Outline each blood parasite and name the species.
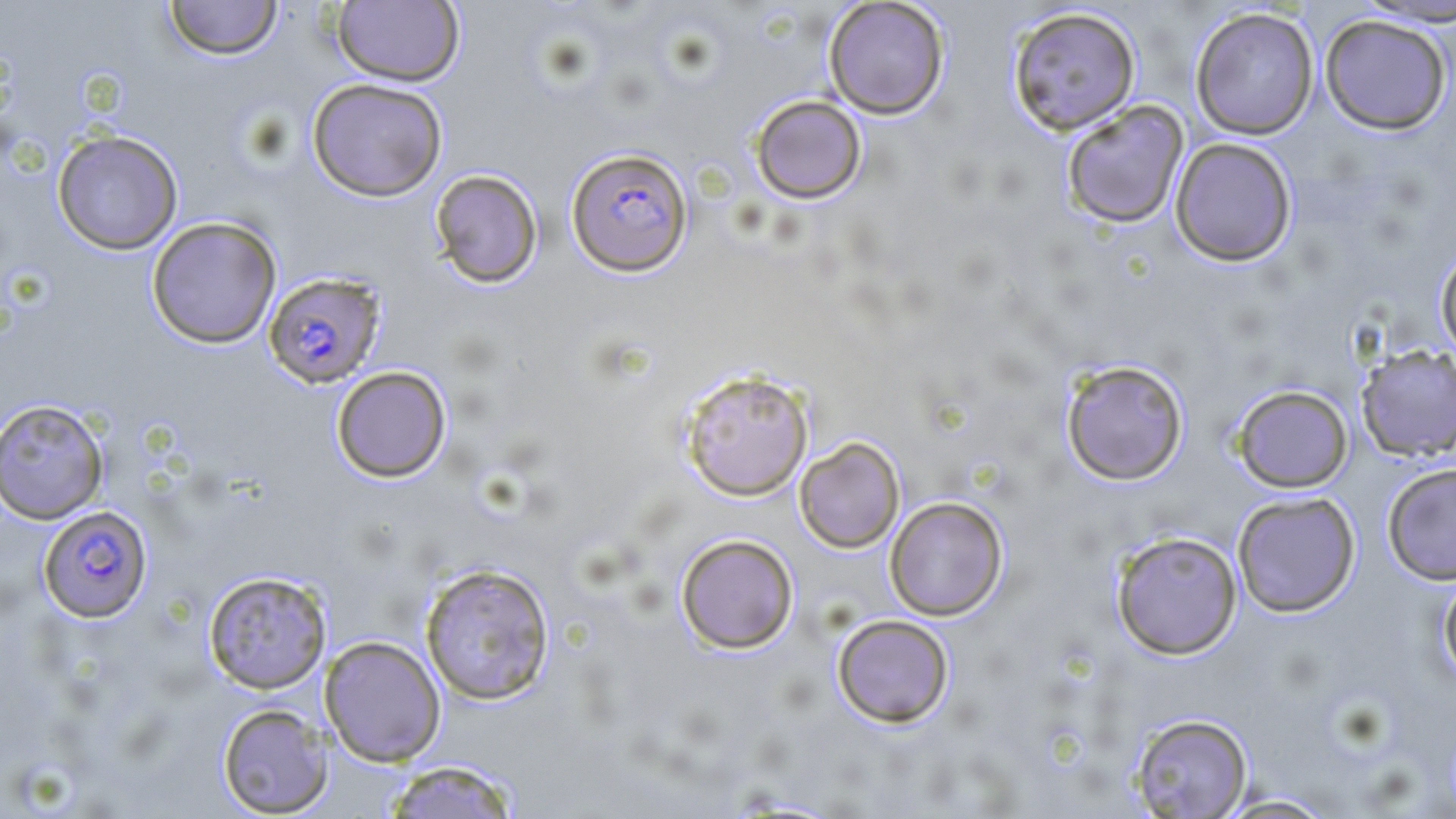
Approximate bounding boxes as [x1, y1, x2, y2] in pixels.
Plasmodium falciparum-infected red blood cells: [566, 147, 693, 276], [263, 271, 387, 388], [38, 505, 153, 622].
No Plasmodium ovale, Plasmodium malariae, Plasmodium vivax, Babesia divergens, or Trypanosoma brucei observed.

Summary:
  - Uninfected red blood cell locations: [163, 0, 283, 60], [333, 0, 465, 87], [823, 0, 950, 119], [1349, 1, 1456, 28], [1007, 6, 1141, 135], [1190, 6, 1320, 140], [1319, 14, 1452, 134], [307, 78, 448, 202], [749, 94, 867, 204], [1061, 99, 1189, 228], [52, 129, 184, 255], [1170, 137, 1297, 267], [429, 169, 543, 288], [146, 216, 282, 349], [1435, 245, 1456, 362], [1356, 344, 1456, 462], [1060, 358, 1189, 486], [331, 365, 451, 483], [679, 368, 814, 501], [1232, 384, 1353, 493], [0, 398, 109, 524], [794, 436, 905, 553], [1382, 462, 1456, 585], [1232, 491, 1361, 617], [885, 496, 1008, 620], [1111, 530, 1242, 659], [675, 534, 799, 653], [419, 562, 556, 706], [203, 570, 332, 694], [1438, 571, 1456, 686], [831, 614, 955, 727], [319, 635, 446, 766], [217, 703, 334, 817], [1128, 713, 1254, 817], [382, 759, 522, 819], [1212, 793, 1341, 818]
  - Slide-level diagnosis: Plasmodium falciparum
  - Stain: May-Grünwald-Giemsa
  - Preparation: thin blood smear
  - Modality: optical microscopy
  - Field of view: single
  - Magnification: 1000x
  - Image size: 1456×819 pixels